Evaluate for malaria.
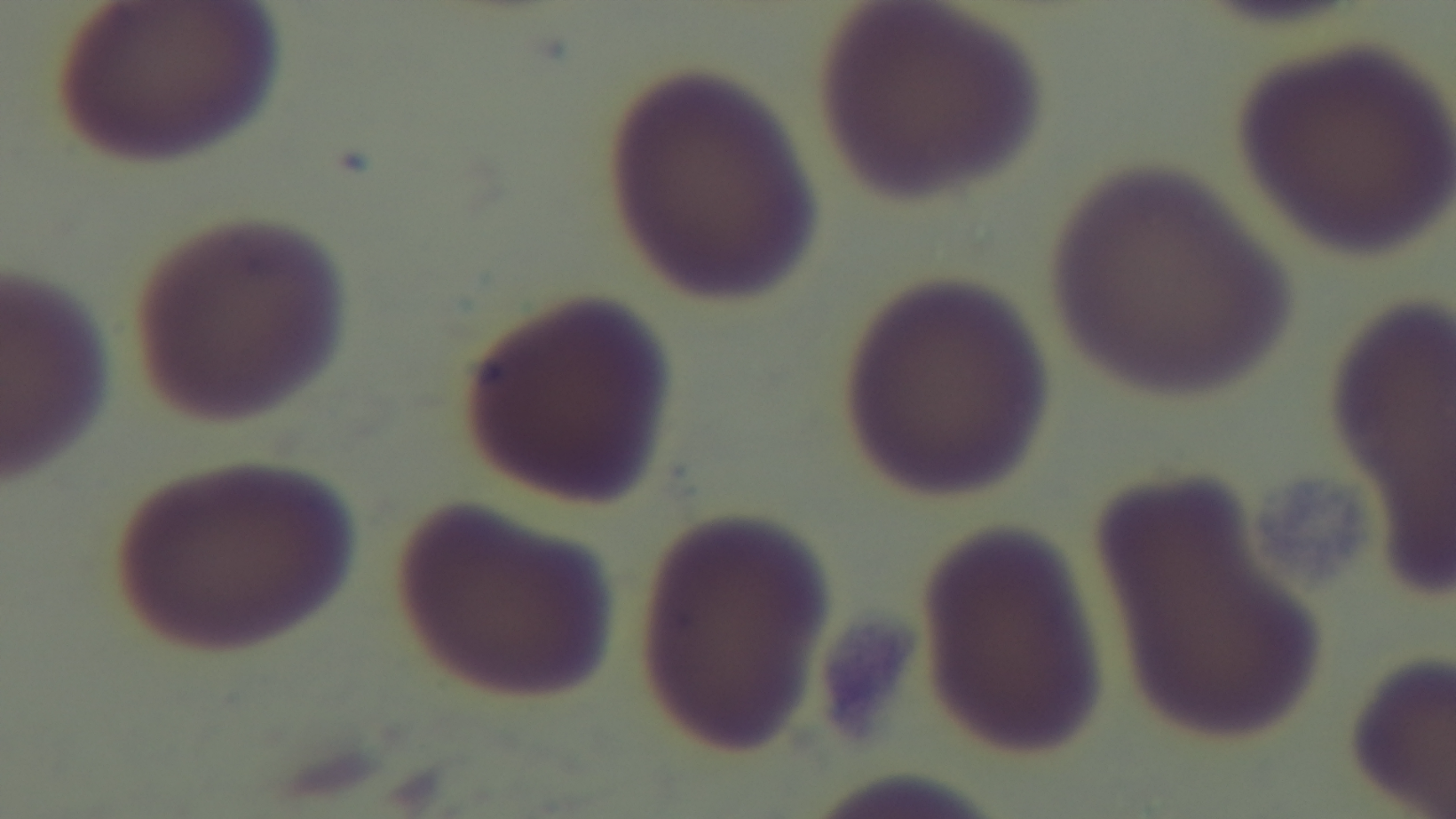

Uninfected.

field of view = single
preparation = thin blood film
stain = Giemsa
capture = mounted 4K digital camera
objective = 100x oil immersion
modality = light microscopy